Locate malaria parasites and leukocytes.
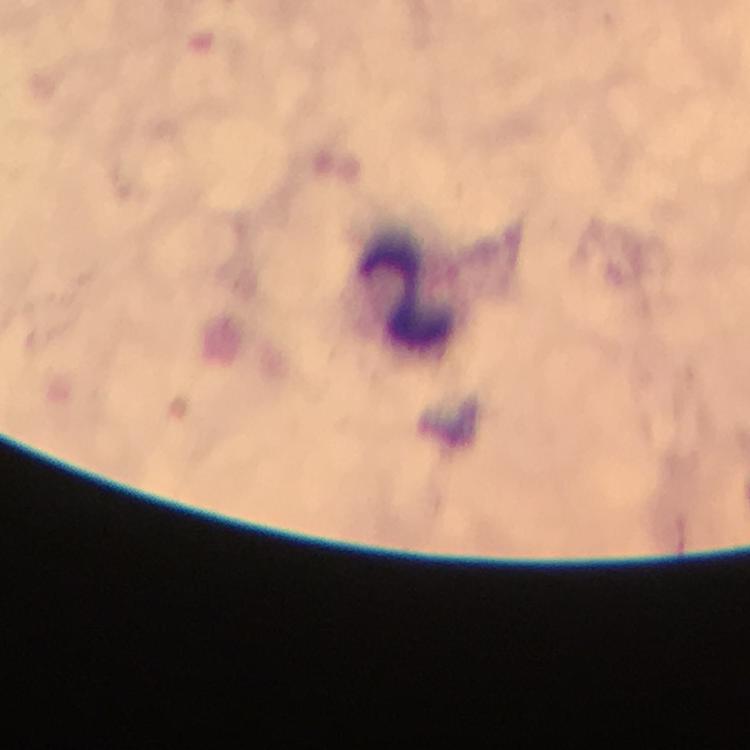

No malaria parasites detected.
Approximate centers as {x, y} in pixels.
Leukocytes: {407, 287}.

Giemsa-stained preparation. Thick smear. At 100x magnification. Cropped region of a single field of view. From a malaria diagnostic workup. Image is 750×750 pixels. Immersion oil was used. Smartphone photograph taken through a microscope.